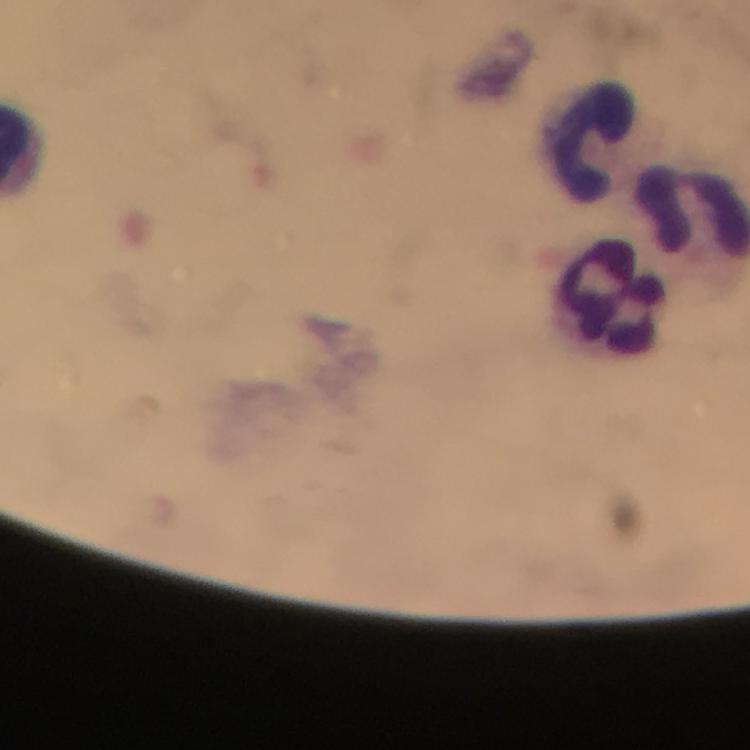
Approximate centers as {x, y} in pixels.
Summary:
  - Leukocyte locations: {588, 142}, {610, 295}
  - Stain: Giemsa
  - Plasmodium parasites: none seen
  - Context: from a diagnostic examination for malaria
  - Cropped from: a single field of view
  - Magnification: 100x
  - Immersion oil: used
  - Preparation: thick blood film
  - Capture: smartphone camera through the microscope
  - Image size: 750×750 pixels